Locate every malaria parasite.
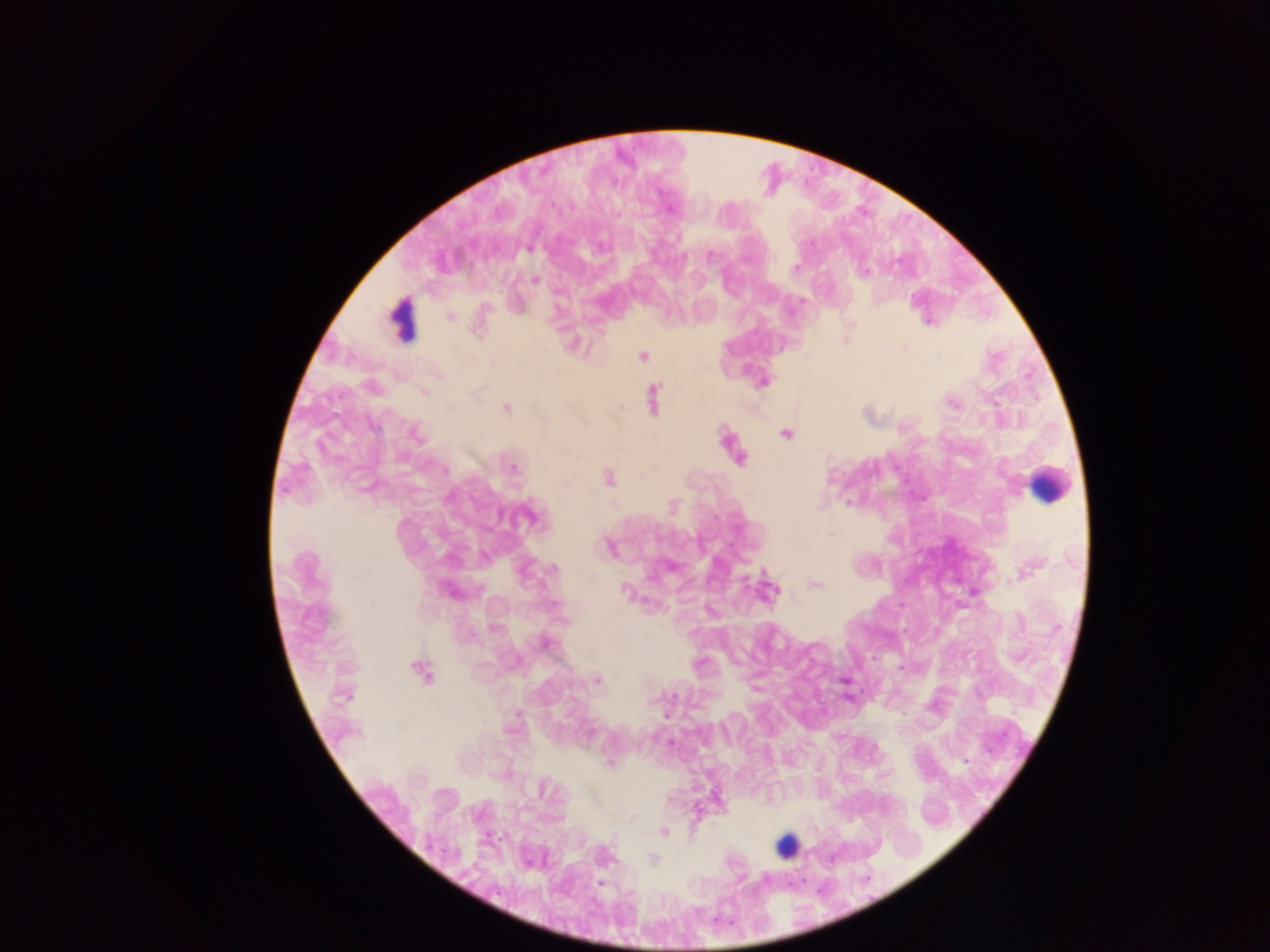

Approximate centers as [x, y] in pixels.
Malaria parasites: [528, 248], [711, 255], [795, 267], [864, 272], [536, 280], [449, 316], [401, 320], [905, 347], [642, 356], [493, 363], [762, 382], [371, 387], [425, 392], [653, 398], [953, 404], [506, 408], [374, 427], [416, 434], [786, 434], [739, 457], [513, 468], [445, 470], [608, 479], [848, 502], [527, 517], [832, 533], [609, 547], [553, 569], [1024, 573], [815, 584], [770, 588], [625, 591], [451, 592], [555, 605], [495, 627], [545, 643], [901, 666], [421, 670], [597, 680], [344, 697], [669, 743], [966, 761], [609, 764], [543, 788], [634, 818], [664, 832], [653, 860], [601, 883].

Leukocyte locations: [1049, 485], [786, 845]. Image is 1270×952 pixels. Thick blood film. Single field of view. Mobile-phone photograph taken through the microscope. Collected in Ghana.